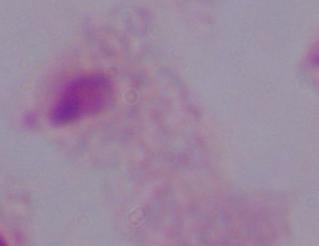
Summary:
  - Identification: trichomonad
  - Magnification: 1000x
  - Modality: photomicrograph